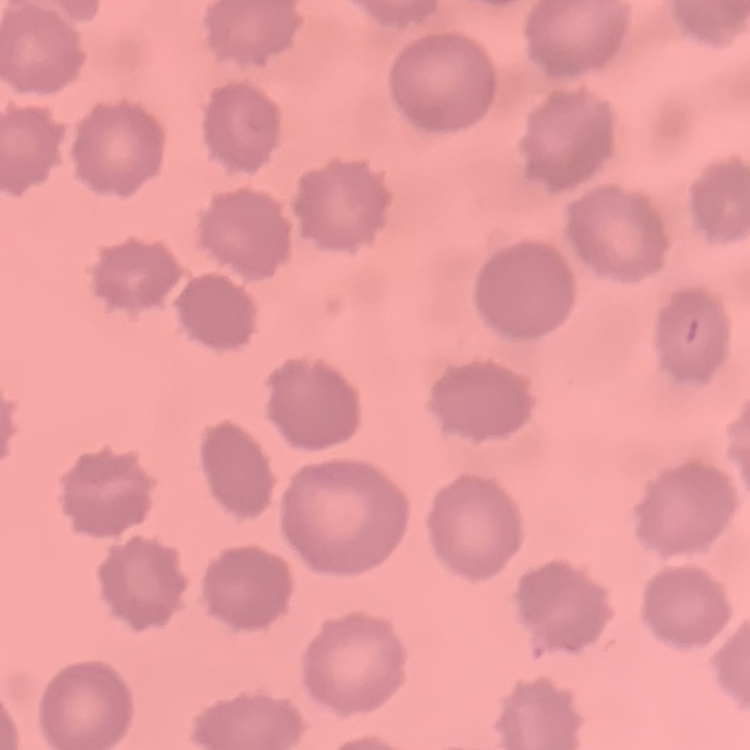
Summary:
  - Erythrocyte morphology: no rouleaux formation
  - Image type: one tile cut from a larger photomicrograph
  - Stain: Field's or Giemsa
  - Preparation: thin blood smear